State which cell type is depicted.
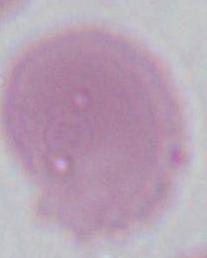
An erythrocyte.

magnification = 1000x
modality = photomicrograph